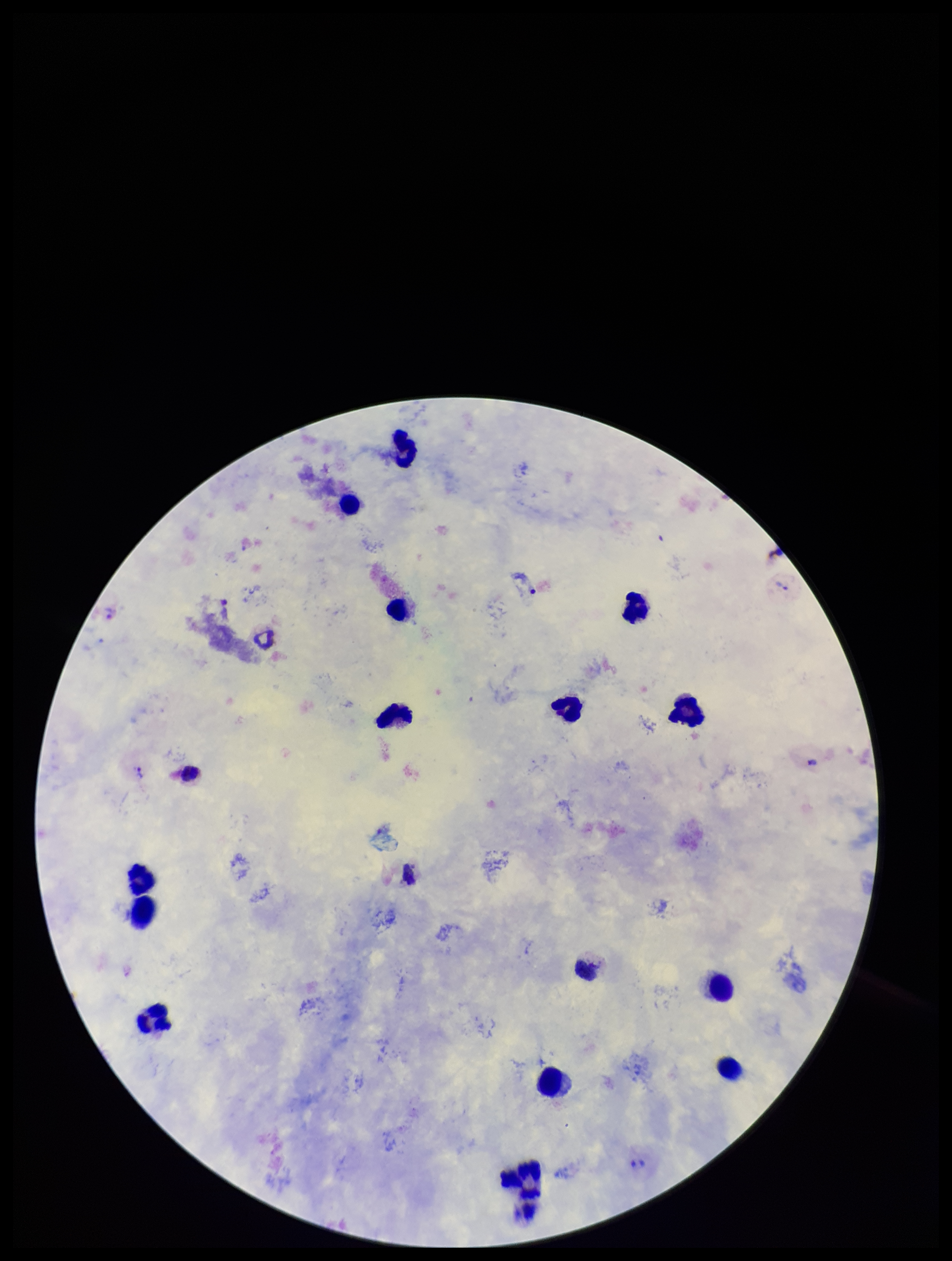
Summary:
  - Species reported for this patient: Plasmodium vivax
  - Capture: smartphone photograph through the microscope eyepiece
  - Parasite count: 3
  - Field of view: single
  - Leukocyte count: 15
  - Stain: Giemsa
  - Preparation: thick
  - Patient malaria status: infected
  - Plasmodium parasites: seen
  - Image size: 952×1261 pixels